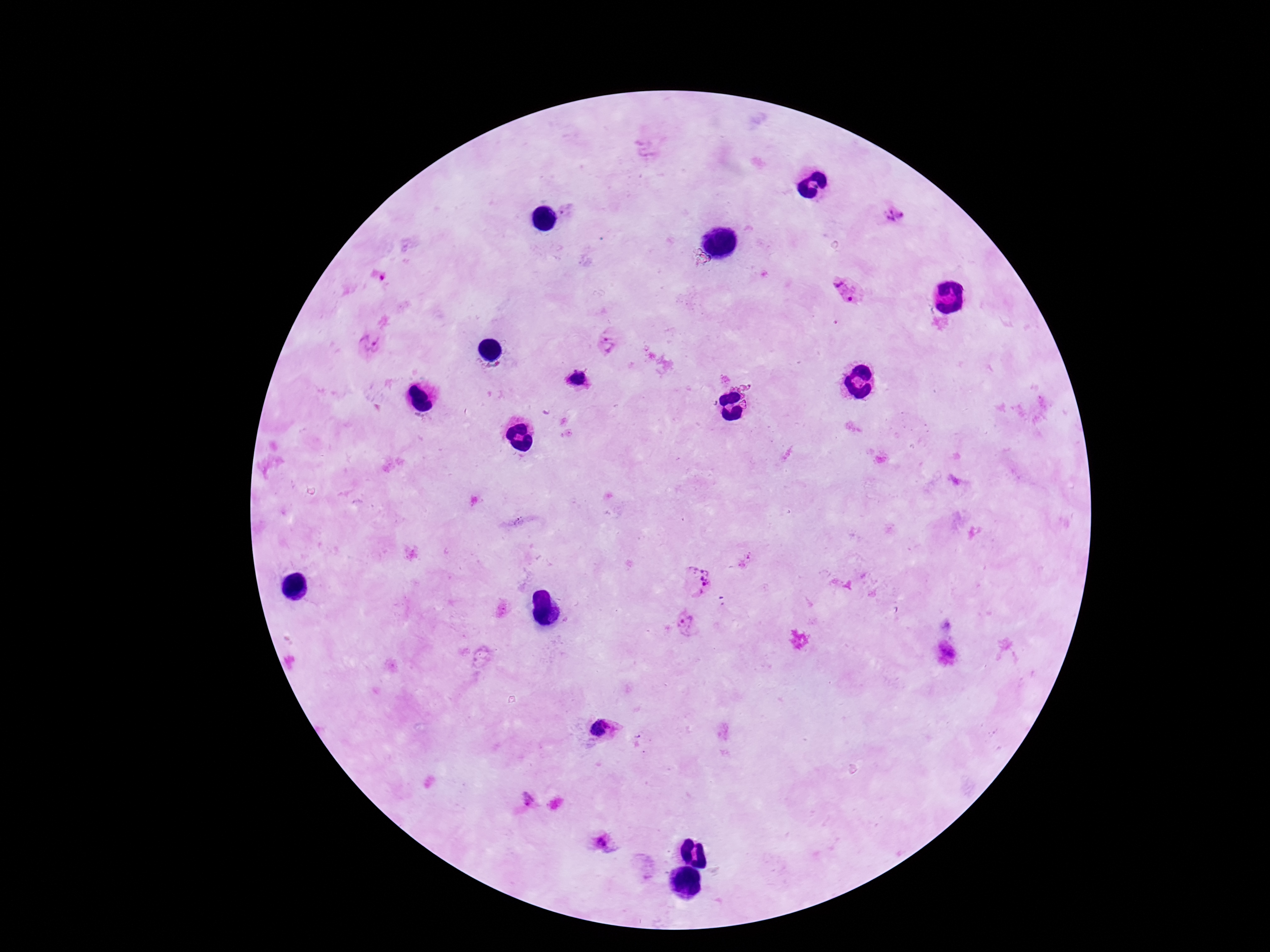
Approximate centers as [x, y] in pixels.
Summary:
  - Plasmodium parasite locations: [895, 214], [379, 276], [844, 290], [611, 343], [371, 345], [578, 379], [745, 560], [699, 579], [686, 622], [947, 652], [602, 729], [529, 798], [600, 837]
  - Field of view: single
  - Image size: 1270×952 pixels
  - Patient malaria status: positive
  - Preparation: thick blood film
  - Capture: smartphone camera through the microscope eyepiece
  - Magnification: 100x
  - Stain: Giemsa